Classify this cell by malaria status.
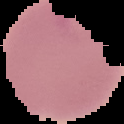

It is parasitized.

image size = 124×124 pixels
image type = segmented cell region on a black background
preparation = thin blood smear